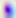
{
  "identification": "Toxoplasma gondii",
  "magnification": "400x",
  "modality": "micrograph"
}